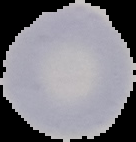 Image is 136×142 pixels. From a thin blood smear. Cell region segmented out of the field of view; the surrounding area is masked to black. Result: no malaria parasites seen.